Assess this cell for malaria.
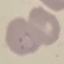

It is parasitized.

Acquired by smartphone through the microscope eyepiece. Giemsa-stained preparation. Automatically extracted cell patch, resized to 64 × 64 pixels. Thin blood film.